Describe the morphology of the red blood cells.
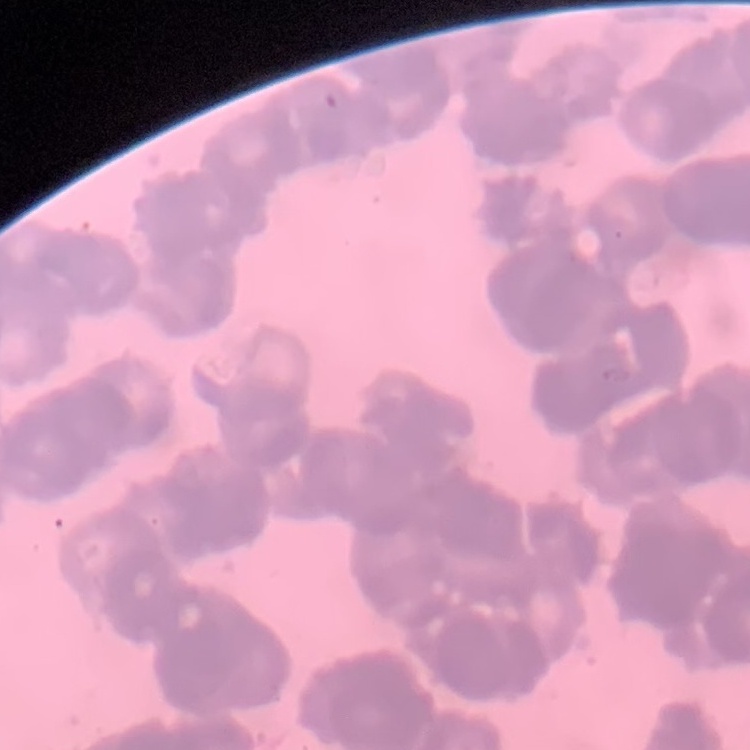

They show rouleaux formation.

preparation: thin peripheral smear
image_type: one tile cut from a larger photomicrograph
stain: Field's or Giemsa